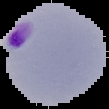 Malaria status: parasitized. From a thin blood smear. Image is 109×109 pixels. Cell region segmented out of the field of view; the surrounding area is masked to black.